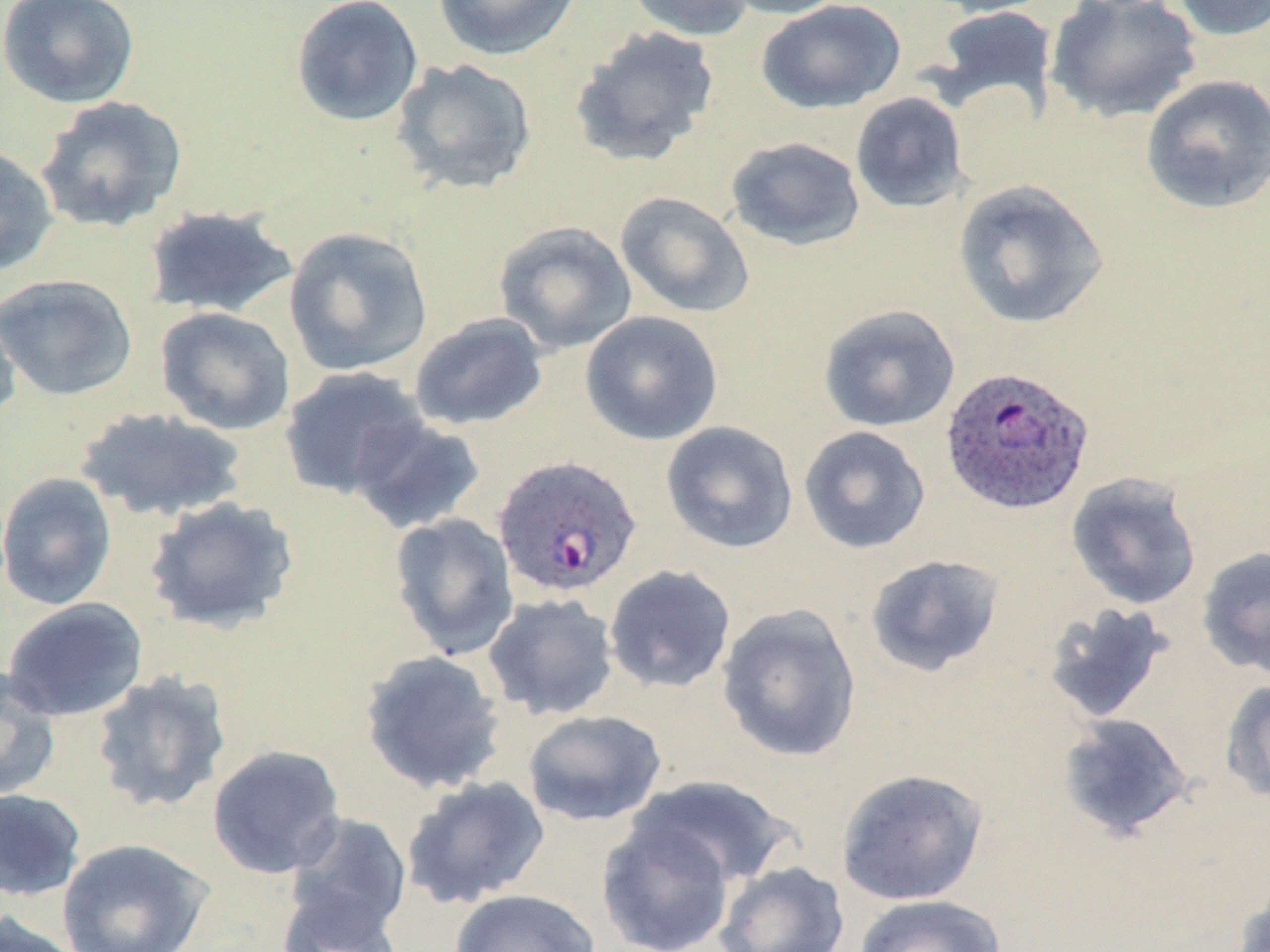

plasmodium_ovale_infected_red_blood_cell_locations: 'approximate bounding boxes as named x1/y1/x2/y2 corners in pixels: (x1=937, y1=369, x2=1093, y2=519), (x1=492, y1=455, x2=643, y2=599)'
slide_level_diagnosis: Plasmodium ovale
uninfected_red_blood_cell_locations: 'approximate bounding boxes as named x1/y1/x2/y2 corners in pixels: (x1=0, y1=0, x2=141, y2=109), (x1=290, y1=0, x2=425, y2=127), (x1=432, y1=0, x2=581, y2=61), (x1=719, y1=0, x2=853, y2=20), (x1=920, y1=0, x2=1057, y2=18), (x1=1169, y1=0, x2=1270, y2=42), (x1=622, y1=1, x2=757, y2=41), (x1=756, y1=1, x2=906, y2=114), (x1=1045, y1=1, x2=1203, y2=125), (x1=928, y1=5, x2=1059, y2=123), (x1=569, y1=25, x2=721, y2=168), (x1=391, y1=58, x2=538, y2=197), (x1=1140, y1=74, x2=1270, y2=215), (x1=850, y1=92, x2=970, y2=214), (x1=34, y1=95, x2=189, y2=233), (x1=725, y1=136, x2=866, y2=252), (x1=0, y1=144, x2=59, y2=277), (x1=952, y1=179, x2=1110, y2=330), (x1=615, y1=191, x2=755, y2=319), (x1=142, y1=205, x2=299, y2=319), (x1=493, y1=220, x2=637, y2=355), (x1=283, y1=226, x2=434, y2=376), (x1=0, y1=273, x2=138, y2=401), (x1=0, y1=300, x2=21, y2=435), (x1=818, y1=304, x2=961, y2=432), (x1=155, y1=306, x2=296, y2=436), (x1=580, y1=310, x2=724, y2=446), (x1=409, y1=312, x2=549, y2=431), (x1=278, y1=366, x2=430, y2=501), (x1=74, y1=406, x2=249, y2=523), (x1=349, y1=416, x2=487, y2=535), (x1=661, y1=421, x2=799, y2=554), (x1=798, y1=426, x2=931, y2=554), (x1=0, y1=472, x2=117, y2=611), (x1=1065, y1=472, x2=1203, y2=611), (x1=143, y1=496, x2=300, y2=634), (x1=389, y1=513, x2=520, y2=660), (x1=1197, y1=546, x2=1270, y2=678), (x1=865, y1=554, x2=1005, y2=678), (x1=604, y1=565, x2=737, y2=693), (x1=482, y1=592, x2=620, y2=721), (x1=2, y1=597, x2=149, y2=723), (x1=1041, y1=601, x2=1175, y2=725), (x1=716, y1=603, x2=862, y2=763), (x1=359, y1=649, x2=507, y2=796), (x1=0, y1=665, x2=61, y2=802), (x1=90, y1=669, x2=232, y2=814), (x1=1221, y1=679, x2=1270, y2=803), (x1=522, y1=709, x2=667, y2=827), (x1=1057, y1=713, x2=1194, y2=841), (x1=207, y1=745, x2=346, y2=879), (x1=836, y1=768, x2=989, y2=906), (x1=629, y1=774, x2=794, y2=888), (x1=401, y1=775, x2=551, y2=910), (x1=0, y1=788, x2=87, y2=902), (x1=283, y1=812, x2=413, y2=941), (x1=596, y1=816, x2=736, y2=952), (x1=56, y1=838, x2=214, y2=952), (x1=714, y1=861, x2=850, y2=952), (x1=1233, y1=881, x2=1270, y2=952), (x1=277, y1=887, x2=405, y2=952), (x1=449, y1=888, x2=601, y2=952), (x1=852, y1=894, x2=1006, y2=952), (x1=0, y1=911, x2=86, y2=952)'
preparation: thin blood film
image_size: 1270×952 pixels
field_of_view: single
modality: light microscopy
magnification: 1000x
stain: May-Grünwald-Giemsa